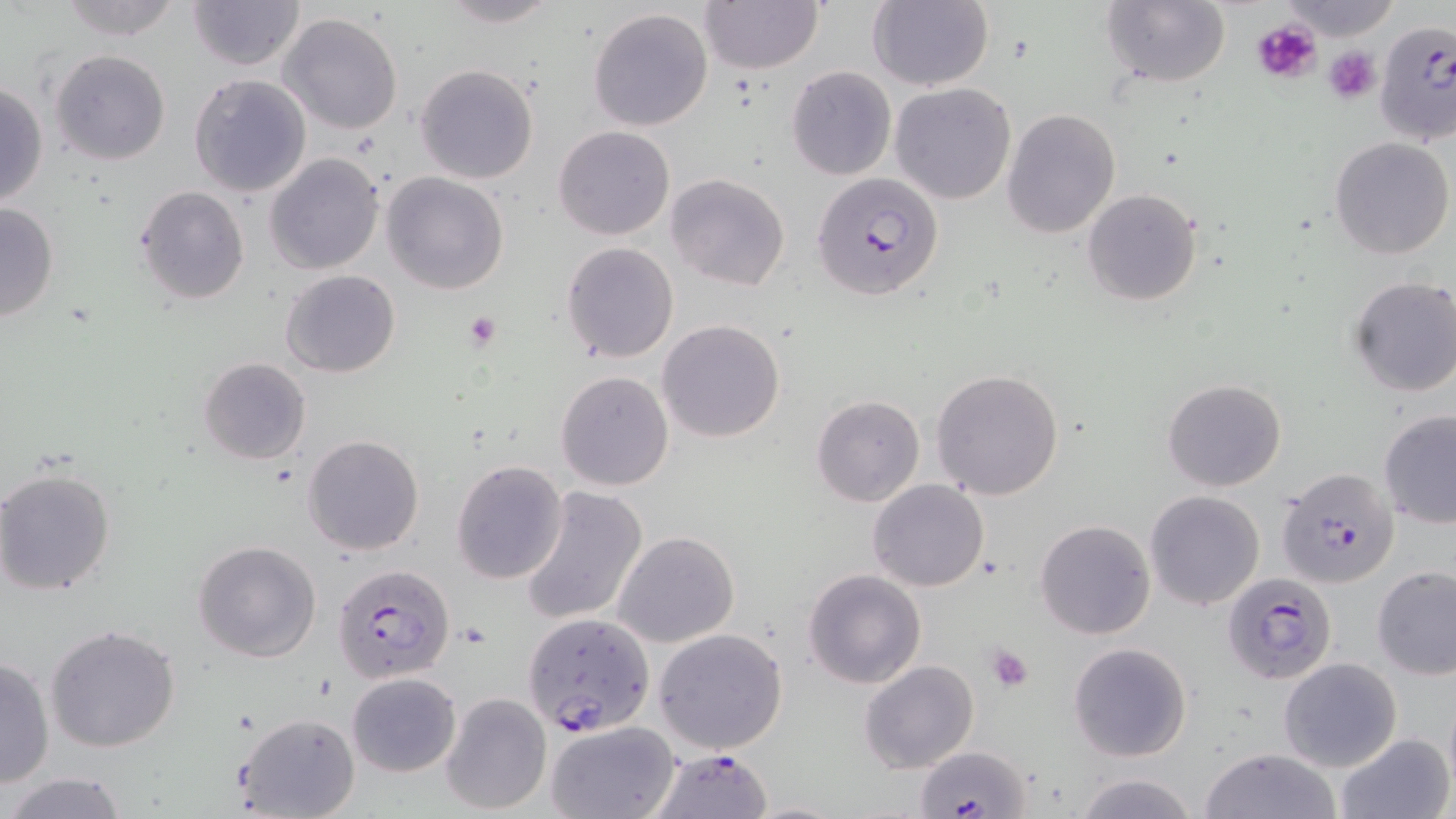

slide-level diagnosis = Plasmodium falciparum
preparation = thin blood smear
field of view = one of a larger specimen
Plasmodium falciparum-infected red blood cell locations = approximate bounding boxes as (x1, y1, x2, y2) in pixels: (1375, 28, 1455, 139), (811, 172, 945, 301), (1276, 467, 1398, 588), (332, 565, 455, 691), (1223, 573, 1338, 684), (525, 611, 654, 737), (916, 746, 1030, 818), (648, 748, 773, 818)
uninfected red blood cell locations = approximate bounding boxes as (x1, y1, x2, y2) in pixels: (56, 0, 185, 41), (435, 0, 563, 27), (699, 0, 823, 72), (866, 0, 994, 90), (1098, 0, 1235, 89), (1281, 0, 1401, 37), (187, 1, 305, 71), (588, 6, 714, 132), (277, 12, 403, 135), (50, 49, 170, 166), (415, 63, 540, 185), (786, 66, 897, 181), (189, 73, 312, 196), (0, 81, 49, 208), (890, 83, 1016, 204), (1003, 108, 1120, 239), (554, 125, 674, 240), (1329, 135, 1454, 259), (265, 152, 385, 274), (381, 171, 509, 295), (666, 173, 791, 291), (134, 185, 250, 304), (1081, 187, 1203, 308), (0, 201, 59, 322), (561, 242, 678, 361), (280, 270, 401, 378), (1347, 276, 1456, 397), (658, 319, 786, 442), (198, 357, 312, 465), (931, 368, 1064, 501), (555, 370, 674, 491), (1162, 379, 1287, 493), (812, 395, 925, 507), (1378, 410, 1456, 528), (302, 435, 424, 556), (450, 458, 568, 584), (1, 466, 117, 596), (868, 479, 989, 592), (520, 488, 648, 627), (1144, 490, 1266, 610), (1035, 519, 1156, 640), (613, 531, 740, 648), (193, 540, 321, 662), (1373, 565, 1456, 679), (804, 569, 927, 689), (46, 624, 181, 754), (653, 628, 789, 754), (1067, 642, 1193, 762), (0, 657, 54, 791), (1278, 657, 1401, 770), (859, 659, 980, 772), (346, 671, 461, 776), (440, 692, 552, 815), (234, 711, 361, 819), (544, 721, 679, 818), (1335, 732, 1454, 819), (1198, 747, 1343, 819), (5, 771, 130, 819), (1073, 771, 1200, 819)
modality = optical microscopy
stain = May-Grünwald-Giemsa
platelet locations = approximate bounding boxes as (x1, y1, x2, y2) in pixels: (1251, 19, 1323, 85), (1325, 48, 1380, 102), (465, 313, 502, 350), (988, 645, 1035, 691)
image size = 1456×819 pixels
magnification = 1000x